Locate Plasmodium falciparum parasites and identify their life-cycle stages.
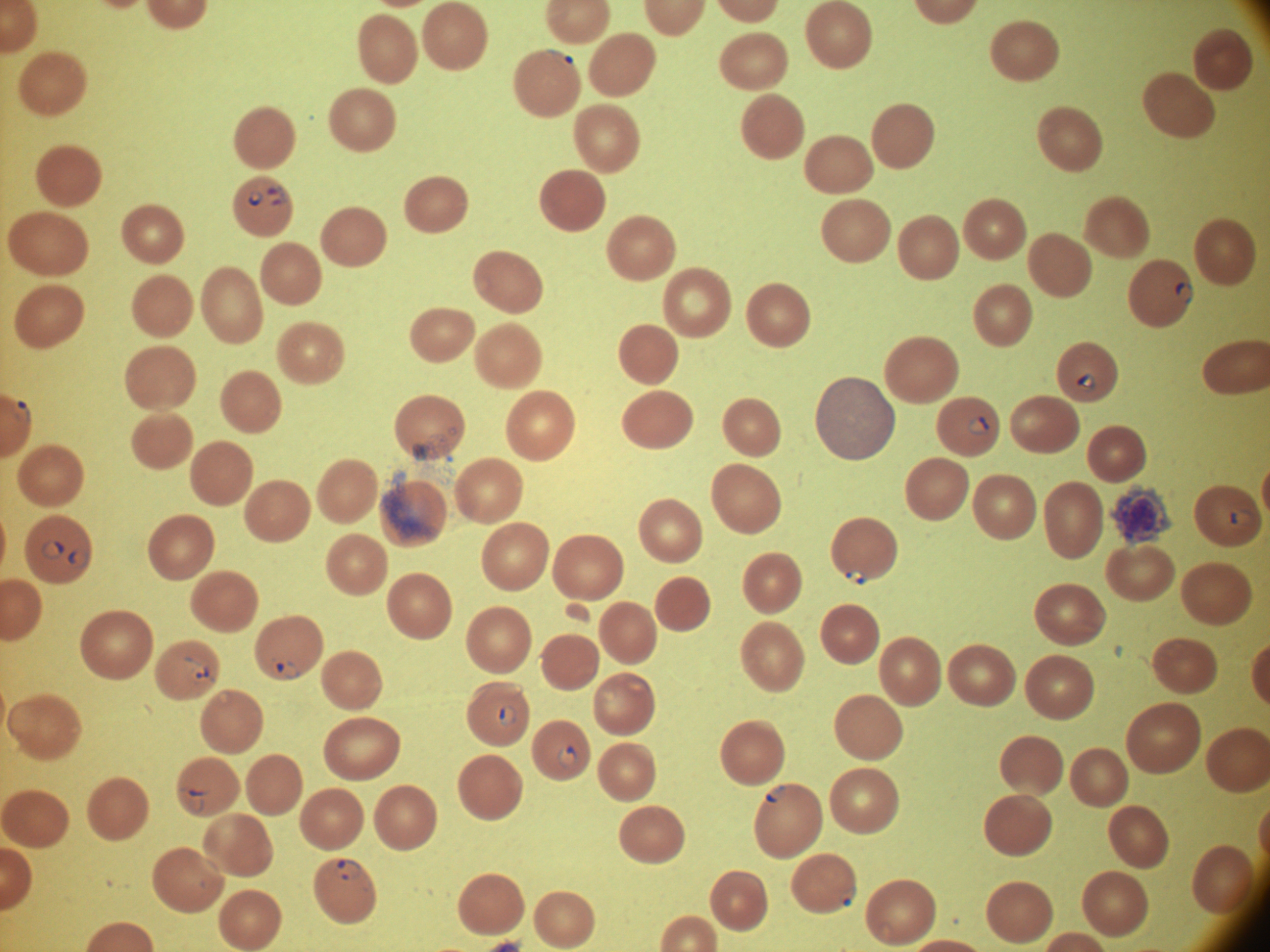
Approximate bounding boxes as [x1, y1, x2, y2] in pixels, from the source annotation, which is not necessarily exhaustive.
Ring forms: [267, 187, 285, 196], [248, 191, 262, 207], [269, 194, 289, 206], [1175, 281, 1194, 304], [1076, 371, 1097, 393], [11, 400, 31, 424], [967, 416, 990, 435], [1230, 509, 1256, 526], [41, 540, 64, 558], [68, 547, 89, 568], [845, 568, 866, 585], [274, 661, 300, 680], [191, 663, 209, 681], [498, 705, 517, 726], [557, 746, 578, 768], [765, 785, 786, 803], [187, 789, 205, 814], [335, 860, 362, 880], [839, 886, 856, 907].

Acquired with a Leica DM2000 optical microscope and its built-in camera. Single field of view. Image is 1270×952 pixels. Thin blood smear. Species: Plasmodium falciparum. 100x magnification. Giemsa stain.